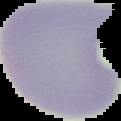
From a thin blood film. Segmented cell region on a black background. Malaria status: uninfected. Image is 121×121 pixels.